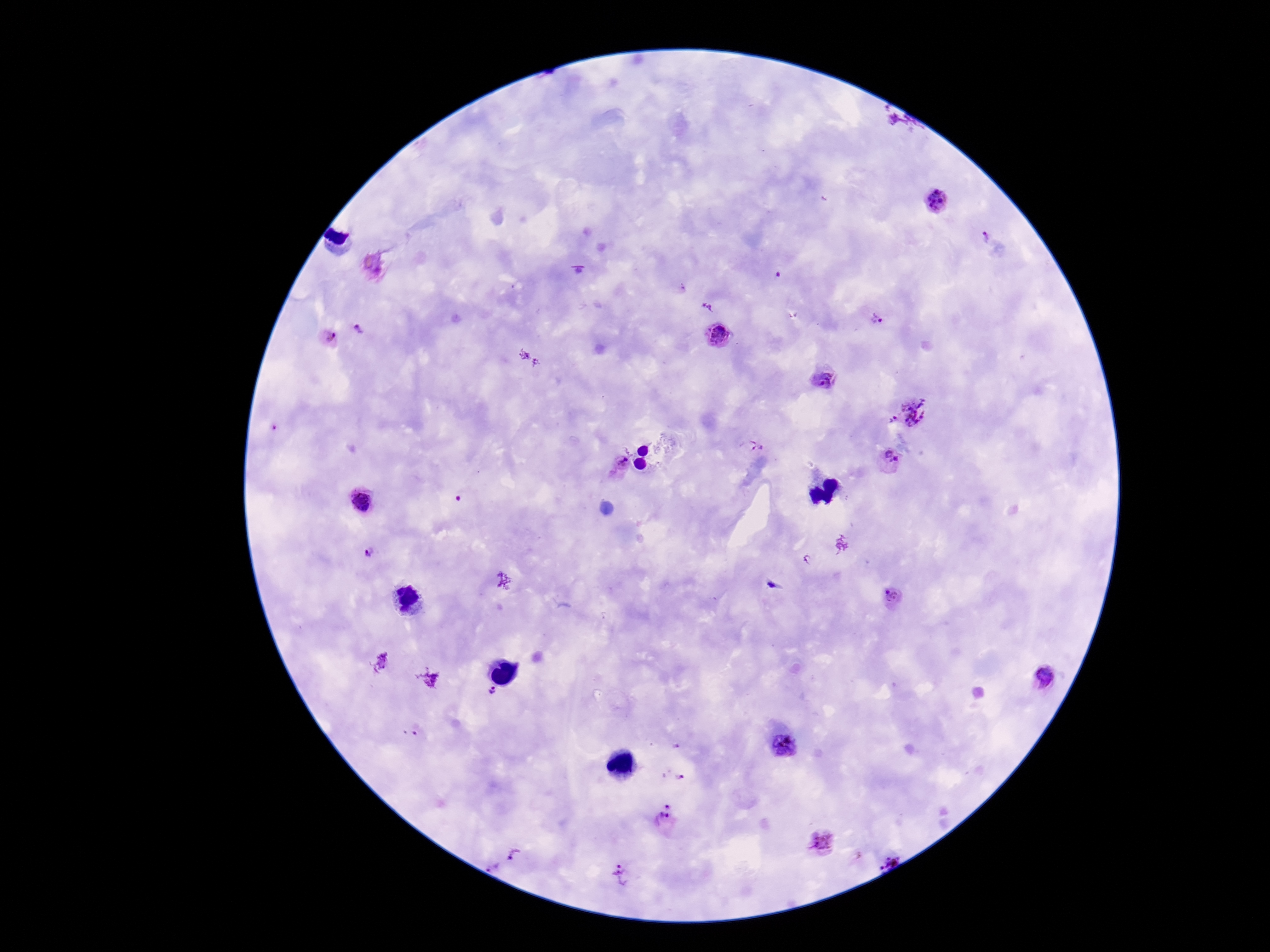
Approximate object centers, in pixels from the top-left corner.
Summary:
  - Plasmodium parasite locations: (x=939, y=201), (x=987, y=235), (x=876, y=320), (x=358, y=327), (x=719, y=335), (x=327, y=339), (x=827, y=378), (x=918, y=410), (x=893, y=419), (x=274, y=427), (x=760, y=445), (x=888, y=459), (x=615, y=467), (x=361, y=500), (x=371, y=553), (x=891, y=598), (x=1047, y=677), (x=493, y=692), (x=419, y=731), (x=784, y=745), (x=675, y=746), (x=678, y=777), (x=667, y=820), (x=822, y=843), (x=516, y=858), (x=888, y=859), (x=621, y=876)
  - Stain: Giemsa
  - Image size: 1270×952 pixels
  - Patient malaria status: positive
  - Capture: smartphone camera through the microscope eyepiece
  - Field of view: single
  - Magnification: 100x
  - Preparation: thick blood film